Assess this cell for malaria.
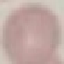
It is uninfected.

Summary:
  - Image type: cell patch, automatically extracted from a larger field of view and resized to 64 × 64 pixels
  - Stain: Giemsa
  - Preparation: thin smear
  - Capture: smartphone through the microscope eyepiece